Evaluate for parasitized red blood cells.
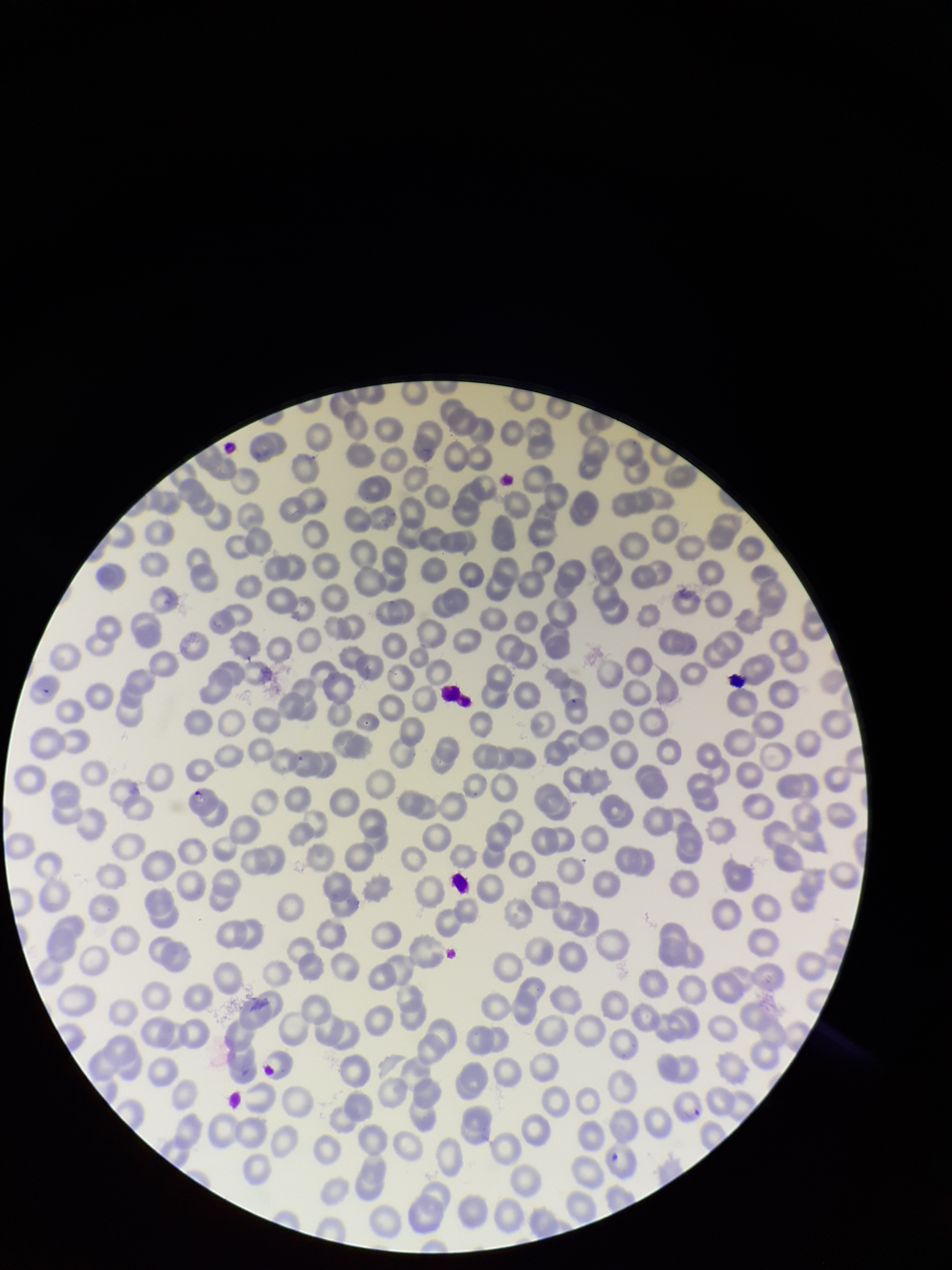
Detected.

{
  "red_blood_cell_count": 255,
  "parasitized_red_blood_cell_count": 1,
  "stain": "Giemsa",
  "image_size": "952×1270 pixels",
  "preparation": "thin smear",
  "field_of_view": "single",
  "capture": "smartphone photograph through the microscope eyepiece",
  "patient_malaria_status": "infected",
  "species_reported_for_this_patient": "Plasmodium falciparum"
}